Describe the morphology of the red blood cells.
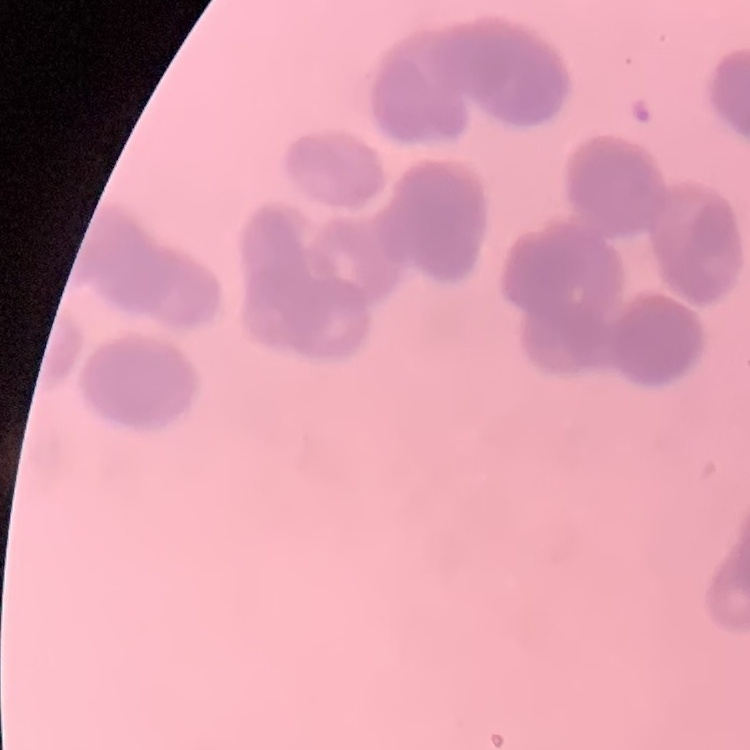

Rouleaux formation.

Summary:
  - Image type: one tile cut from a larger photomicrograph
  - Stain: Field's or Giemsa
  - Preparation: thin blood smear